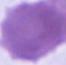
Summary:
  - Magnification: 1000x
  - Modality: micrograph
  - Identification: erythrocyte